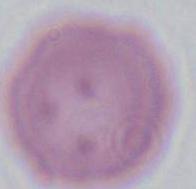 Micrograph. An erythrocyte is shown. 1000x magnification.